State which parasite is depicted.
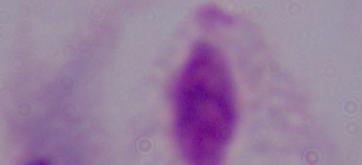
This is a trichomonad.

modality = micrograph
magnification = 1000x